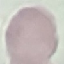
{
  "malaria_status": "uninfected",
  "image_type": "cell patch, automatically extracted from a larger field of view and resized to 64 × 64 pixels",
  "preparation": "thin smear",
  "capture": "smartphone through the microscope eyepiece",
  "stain": "Giemsa"
}